Outline each Plasmodium vivax-infected red blood cell.
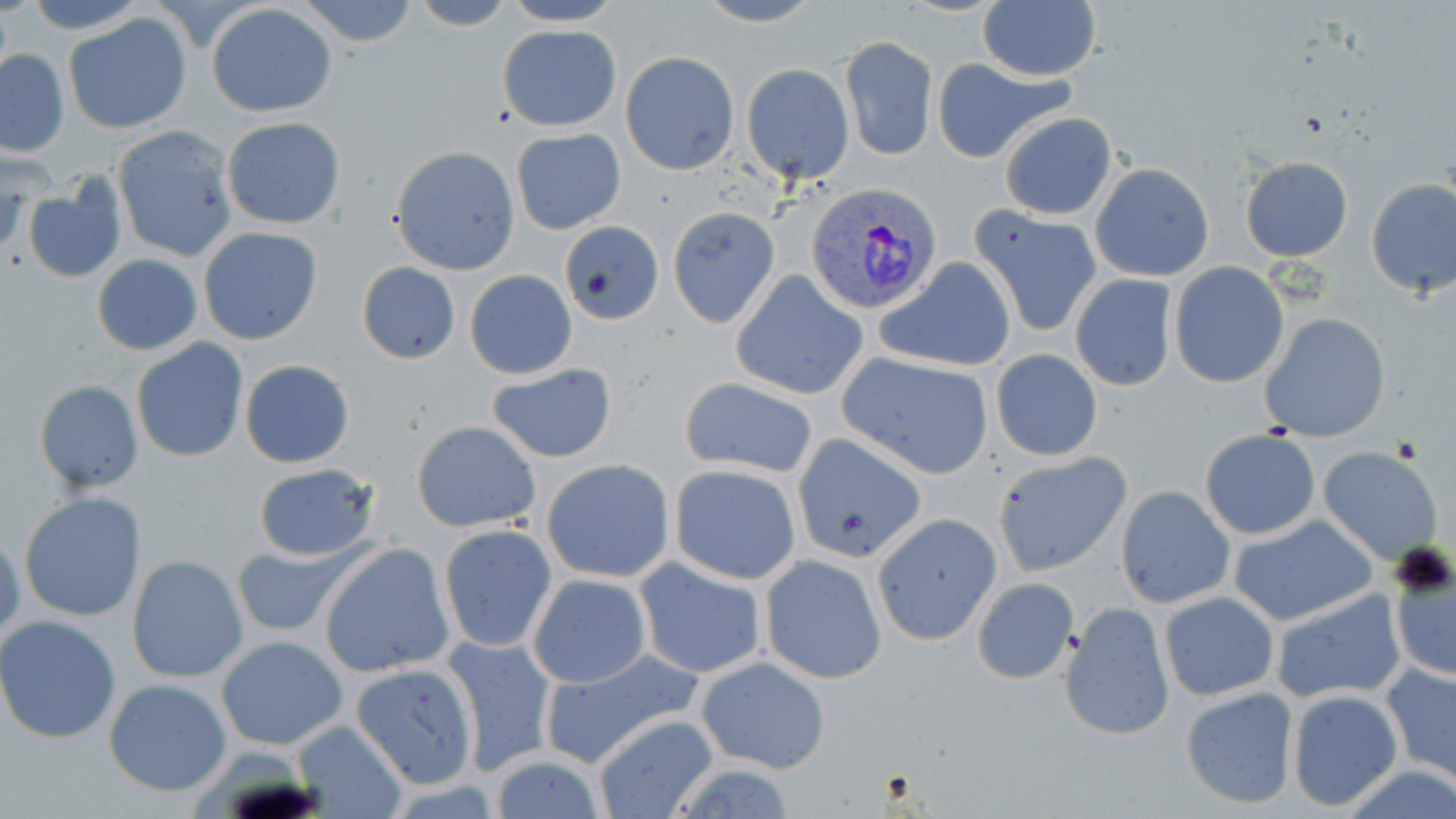
Approximate bounding boxes as (x1,y1)-(x2,y2) corner pairs in pixels.
Plasmodium vivax-infected red blood cells: (806,183)-(944,317).

Uninfected red blood cell locations: (18,0)-(158,32), (294,0)-(422,47), (406,0)-(519,30), (498,0)-(626,26), (691,0)-(826,27), (977,2)-(1101,81), (207,3)-(338,118), (65,13)-(192,134), (497,25)-(621,131), (840,36)-(937,162), (1,48)-(69,156), (621,51)-(739,175), (930,57)-(1073,162), (742,64)-(854,184), (999,111)-(1119,220), (220,117)-(345,231), (112,125)-(238,262), (511,127)-(626,235), (995,129)-(1200,246), (390,147)-(520,275), (1240,156)-(1352,262), (1092,162)-(1215,280), (1365,178)-(1456,298), (23,183)-(126,283), (969,203)-(1101,338), (667,207)-(781,329), (559,223)-(662,325), (198,226)-(323,345), (91,254)-(202,356), (875,257)-(1017,374), (356,263)-(461,365), (1169,263)-(1288,387), (730,269)-(867,400), (465,270)-(577,380), (1069,274)-(1176,392), (1261,312)-(1391,442), (132,339)-(247,462), (989,348)-(1103,462), (836,351)-(995,480), (239,358)-(355,469), (484,362)-(618,465), (680,377)-(819,479), (33,380)-(144,494), (412,420)-(541,533), (1200,429)-(1321,539), (791,432)-(930,564), (1318,447)-(1446,567), (990,451)-(1132,578), (540,459)-(675,582), (251,461)-(384,563), (669,464)-(802,585), (1115,486)-(1234,609), (19,491)-(148,622), (871,513)-(1001,646), (1229,514)-(1377,627), (437,525)-(557,652), (1,529)-(24,649), (233,541)-(362,640), (319,543)-(454,678), (1386,551)-(1455,682), (127,555)-(247,681), (759,555)-(888,683), (634,558)-(767,679), (527,573)-(652,687), (973,577)-(1078,684), (1268,587)-(1405,705), (1160,592)-(1279,703), (1059,601)-(1173,741), (0,617)-(122,741), (216,635)-(348,751), (441,636)-(556,777), (541,651)-(703,767), (695,656)-(832,775), (350,663)-(480,789), (1382,663)-(1456,783), (103,678)-(231,797), (1179,686)-(1299,811), (1285,689)-(1403,812), (591,714)-(718,818), (291,719)-(407,818), (488,757)-(609,819). Platelet locations: (1389,541)-(1455,599). Slide-level diagnosis: Plasmodium vivax. Single field of view. Captured at 1000x magnification. Image is 1456×819 pixels. Light microscopy. May-Grünwald-Giemsa-stained preparation. Thin blood smear.